Report the malaria status of this cell.
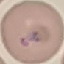
Parasitized.

Cell patch, automatically extracted from a larger field of view and resized to 64 × 64 pixels. Acquired by smartphone through the microscope eyepiece. Giemsa-stained preparation. Thin blood film.